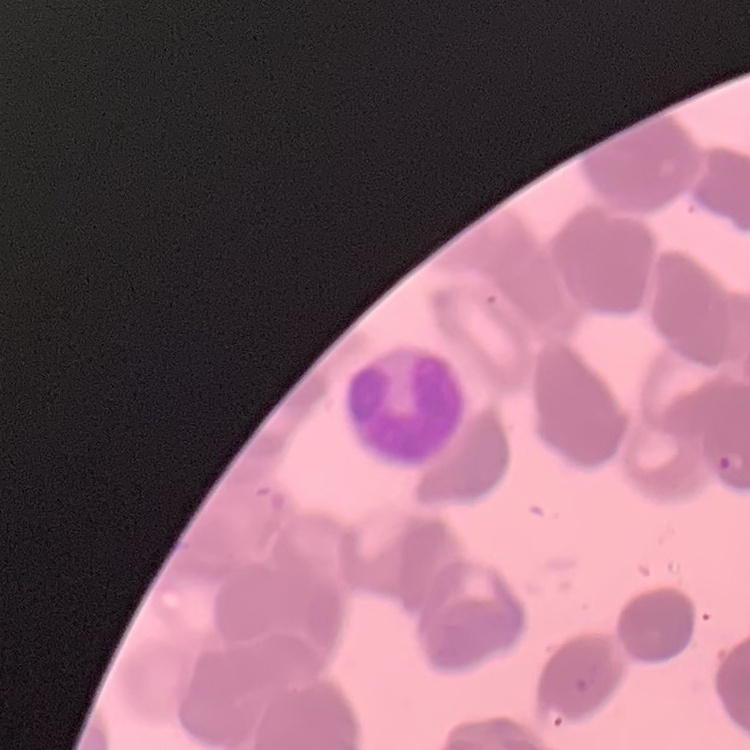
red blood cell morphology = rouleaux formation
image type = one tile cut from a larger photomicrograph
preparation = thin blood film
stain = Field's or Giemsa